Classify this cell by malaria status.
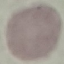
It is uninfected.

Cell patch, automatically extracted from a larger field of view and resized to 64 × 64 pixels. Acquired by smartphone through the microscope eyepiece. Giemsa stain. Thin blood film.